Identify the cell.
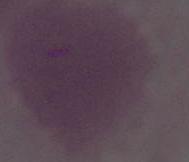
This is an erythrocyte.

modality = micrograph
magnification = 1000x